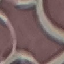

Result: negative for malaria parasites. Giemsa stain. Automatically extracted cell patch, resized to 64 × 64 pixels. Photographed with a smartphone camera at the microscope eyepiece. Thin smear of blood.